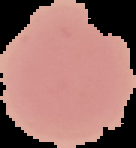

Summary:
  - Image type: segmented cell region with the area outside set to black
  - Preparation: thin blood smear
  - Image size: 136×148 pixels
  - Result: no Plasmodium parasites detected